Describe the morphology of the erythrocytes.
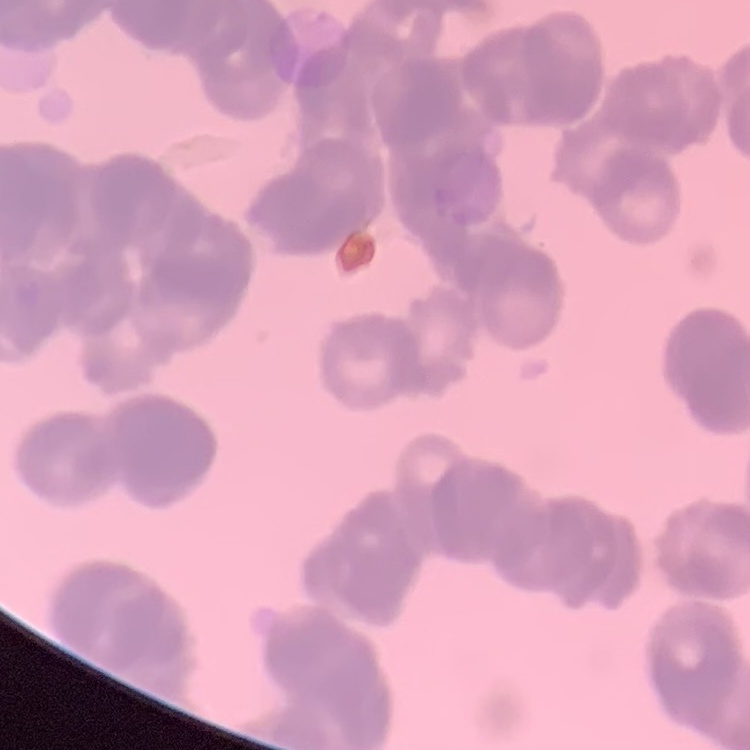

Rouleaux formation.

Field's or Giemsa stain. Thin blood smear. One tile cut from a larger photomicrograph.